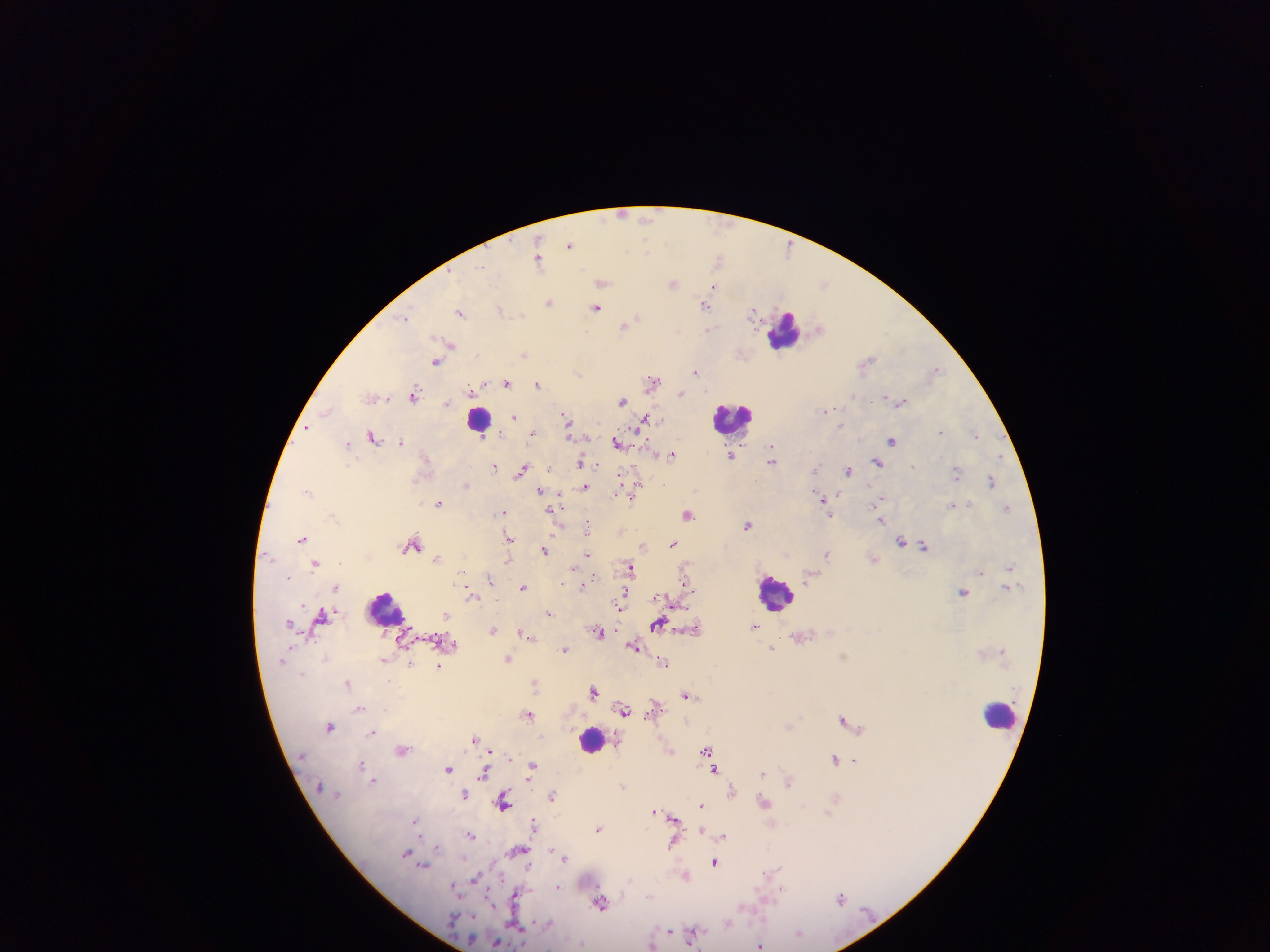
country = Ghana
capture = mobile-phone photograph through a microscope
field of view = single
image size = 1270×952 pixels
preparation = thick blood film
leukocyte locations = approximate centers as x y in pixels: 783 330; 731 419; 478 423; 772 591; 385 609; 1001 717; 591 740
Plasmodium parasite locations = approximate centers as x y in pixels: 621 216; 646 219; 646 244; 570 245; 717 257; 538 258; 605 283; 673 284; 824 284; 714 286; 549 304; 596 307; 704 307; 460 312; 751 313; 639 317; 407 319; 623 327; 708 329; 451 344; 525 353; 871 357; 435 361; 936 368; 696 372; 579 373; 505 382; 653 383; 537 384; 415 392; 681 394; 450 401; 623 401; 901 401; 828 408; 514 416; 563 416; 646 417; 568 422; 842 423; 306 430; 940 431; 532 432; 568 435; 373 436; 977 436; 892 440; 401 441; 617 443; 347 444; 770 445; 731 455; 671 456; 878 461; 580 462; 771 463; 915 464; 496 465; 595 467; 522 468; 848 469; 814 470; 622 474; 957 474; 637 477; 989 481; 639 483; 663 484; 466 485; 540 489; 586 489; 307 492; 615 493; 560 495; 632 495; 882 496; 821 498; 438 502; 968 504; 953 505; 564 507; 1007 507; 828 511; 503 512; 550 513; 688 514; 829 517; 882 520; 587 526; 749 527; 303 537; 508 538; 900 542; 673 543; 643 545; 925 546; 414 547; 406 550; 543 551; 588 553; 827 554; 438 558; 270 559; 507 559; 316 564; 575 565; 630 565; 1009 566; 982 572; 289 576; 489 580; 684 580; 461 582; 562 583; 582 584; 688 586; 522 587; 963 593; 622 594; 473 598; 667 598; 675 603; 307 607; 681 607; 621 608; 322 613; 550 613; 447 614; 291 623; 657 624; 495 630; 521 631; 599 632; 634 647; 774 648; 566 649; 845 655; 510 659; 661 662; 439 666; 536 681; 347 683; 593 691; 686 694; 359 709; 621 709; 626 711; 529 713; 844 718; 789 725; 329 726; 373 733; 473 738; 490 750; 707 750; 834 758; 853 759; 360 765; 533 765; 449 769; 716 770; 763 772; 482 773; 374 781; 789 782; 318 786; 463 796; 552 796; 836 796; 504 802; 765 802; 702 804; 804 805; 655 812; 829 813; 417 818; 677 819; 536 823; 598 830; 471 833; 725 837; 672 844; 438 846; 551 850; 406 851; 525 851; 565 860; 527 862; 714 862; 426 867; 777 868; 685 876; 475 878; 558 886; 454 888; 782 889; 515 892; 648 896; 841 896; 488 898; 766 898; 767 901; 600 905; 743 907; 670 930; 693 937; 496 941; 760 943